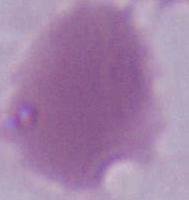

An erythrocyte is shown. Captured at 1000x magnification. Micrograph.